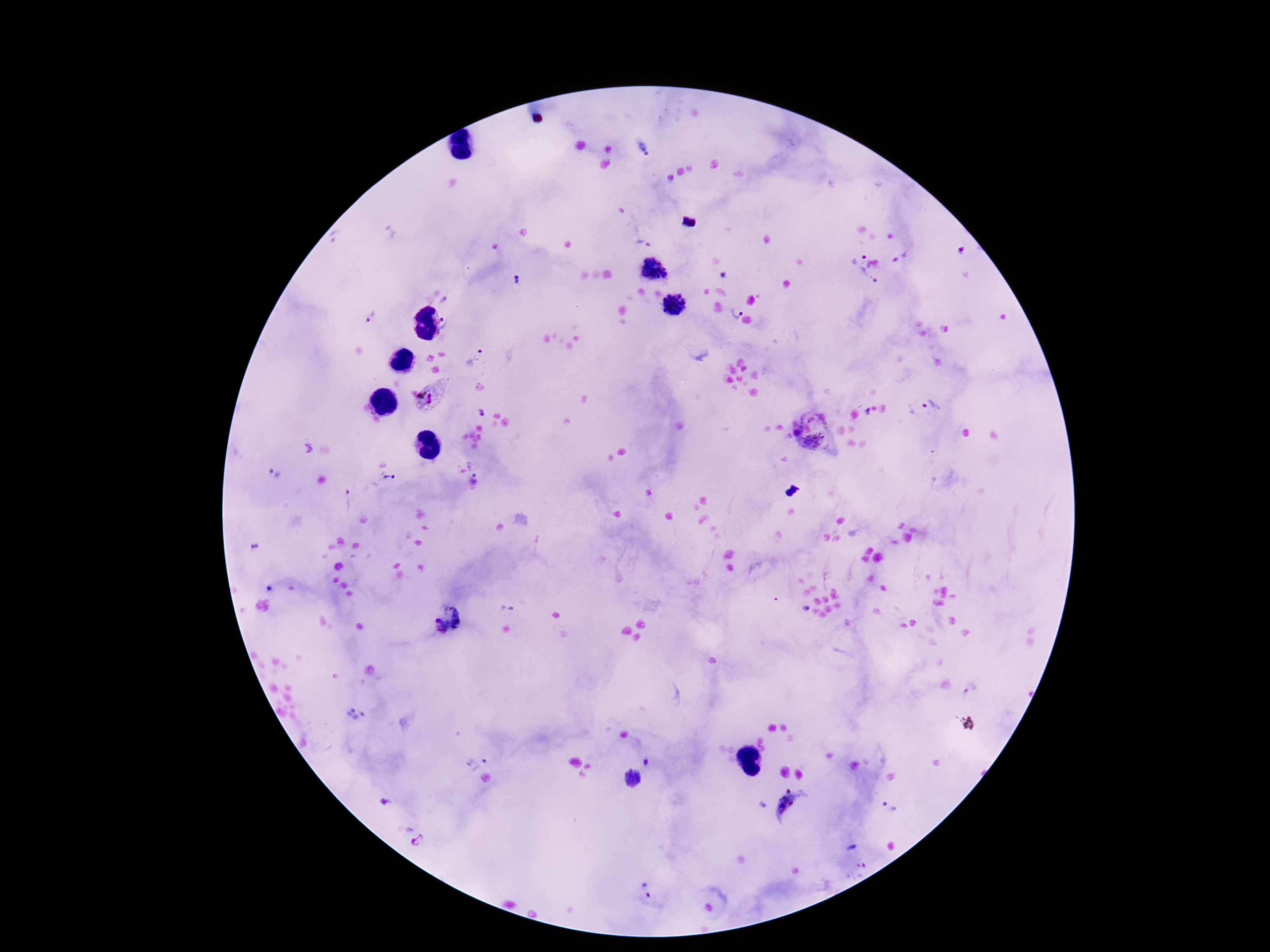
Approximate centers as [x, y] in pixels.
Summary:
  - Plasmodium parasite locations: [643, 147], [644, 242], [962, 251], [857, 256], [653, 268], [723, 275], [868, 278], [518, 279], [444, 301], [674, 306], [735, 311], [372, 317], [449, 323], [475, 357], [435, 395], [930, 406], [866, 411], [813, 415], [797, 432], [814, 444], [273, 473], [388, 477], [479, 478], [347, 500], [254, 546], [269, 589], [507, 608], [806, 608], [446, 620], [970, 689], [357, 715], [475, 758], [647, 761], [632, 778], [387, 801], [762, 805], [792, 805], [888, 807], [418, 839], [852, 847], [646, 888]
  - Stain: Giemsa
  - Magnification: 100x
  - Preparation: thick blood smear
  - Patient malaria status: positive
  - Capture: smartphone camera through the microscope eyepiece
  - Image size: 1270×952 pixels
  - Field of view: single